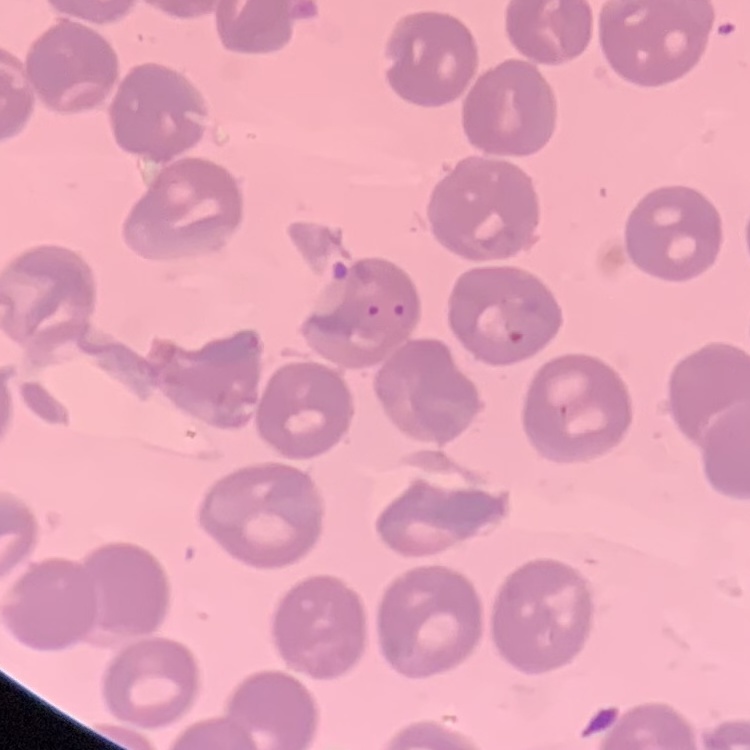

{
  "red_blood_cell_morphology": "no rouleaux formation",
  "stain": "Field's or Giemsa",
  "image_type": "one tile cut from a larger photomicrograph",
  "preparation": "thin blood smear"
}